Assess the morphology of the erythrocytes.
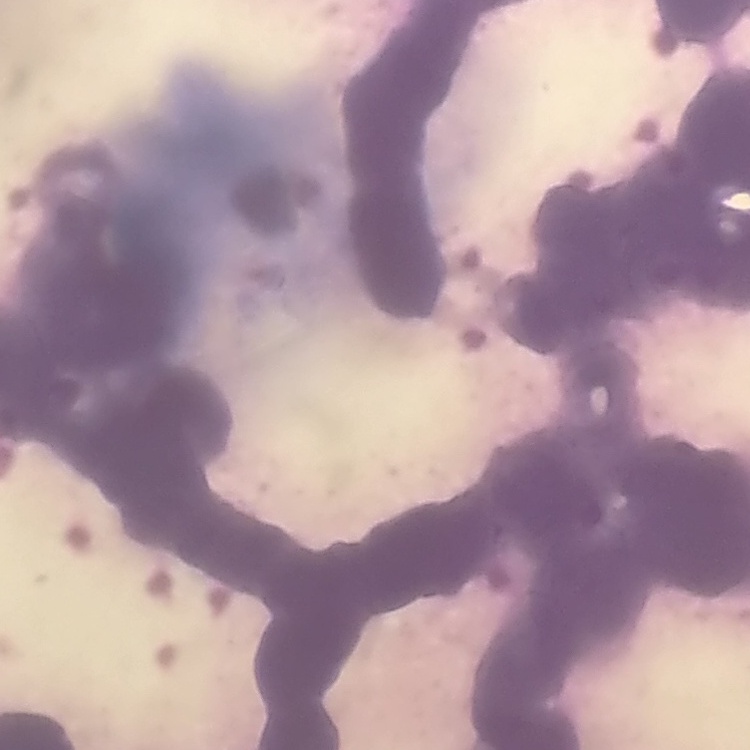

Rouleaux formation.

Stained with either Field's or Giemsa. Square crop of a larger photomicrograph. Thin blood smear.